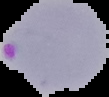

Summary:
  - Image type: segmented cell region with the area outside set to black
  - Image size: 109×97 pixels
  - Preparation: thin blood film
  - Malaria status: parasitized